Assess the morphology of the erythrocytes.
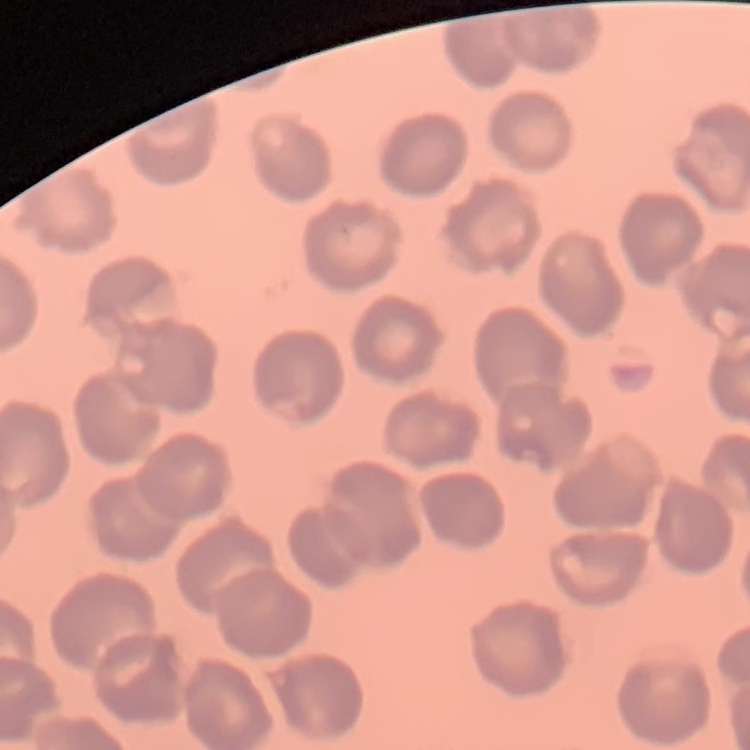

They show no rouleaux formation.

Square crop of a larger photomicrograph. Thin peripheral smear. Stained with either Field's or Giemsa.